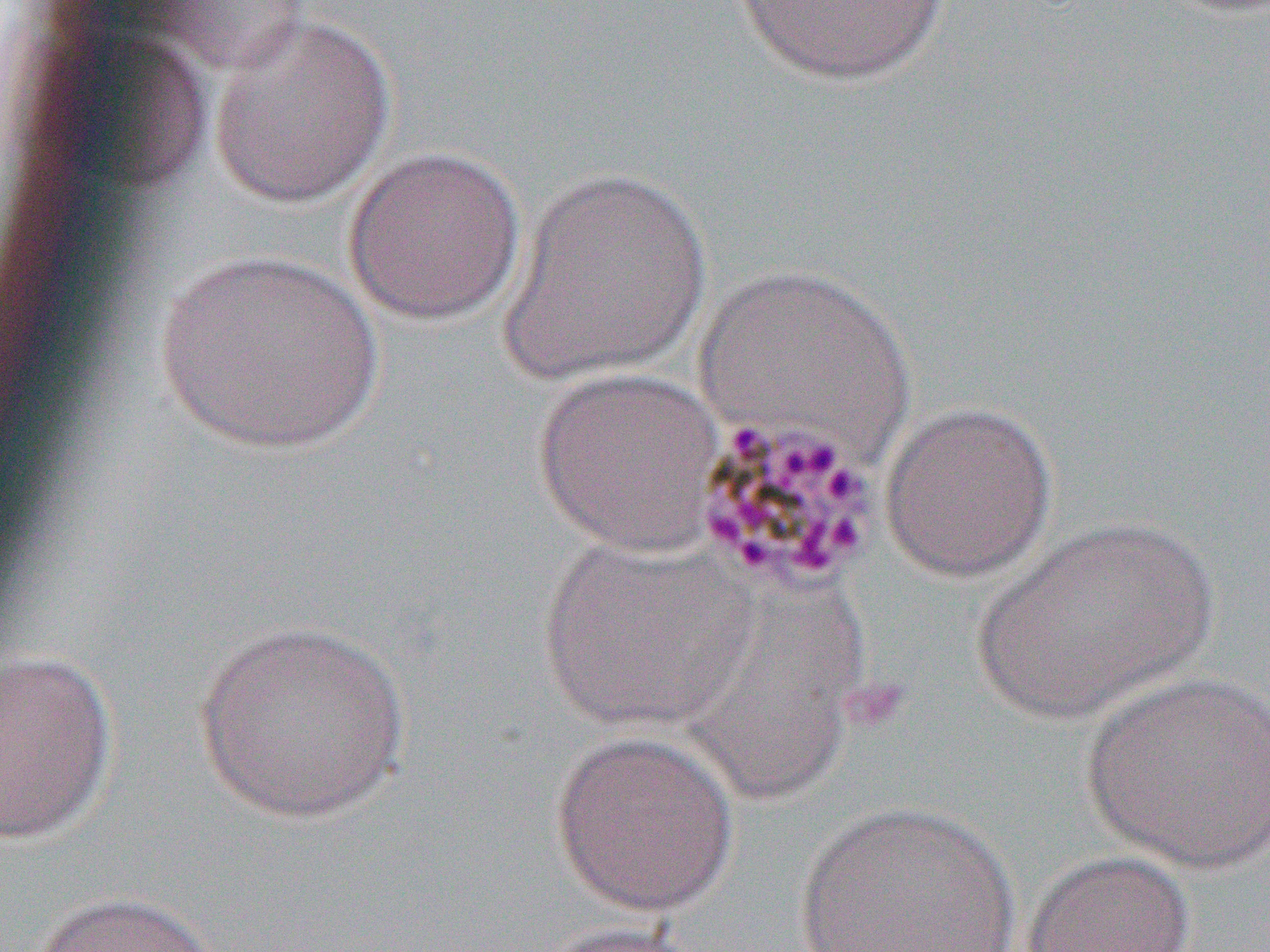

Summary:
  - Coordinate format: approximate bounding boxes as named x1/y1/x2/y2 corners in pixels
  - Uninfected red blood cell locations: (x1=729, y1=0, x2=951, y2=86), (x1=207, y1=13, x2=396, y2=209), (x1=342, y1=145, x2=528, y2=326), (x1=500, y1=163, x2=712, y2=386), (x1=151, y1=250, x2=386, y2=453), (x1=695, y1=263, x2=915, y2=466), (x1=533, y1=366, x2=726, y2=557), (x1=878, y1=399, x2=1058, y2=583), (x1=971, y1=516, x2=1219, y2=723), (x1=537, y1=533, x2=759, y2=731), (x1=194, y1=619, x2=410, y2=824), (x1=1, y1=649, x2=119, y2=845), (x1=1079, y1=670, x2=1270, y2=872), (x1=548, y1=729, x2=741, y2=916), (x1=791, y1=800, x2=1022, y2=951), (x1=1022, y1=849, x2=1197, y2=952), (x1=25, y1=890, x2=228, y2=952), (x1=532, y1=920, x2=708, y2=952)
  - Slide-level diagnosis: Plasmodium malariae
  - Image size: 1270×952 pixels
  - Magnification: 1000x
  - Modality: light microscopy
  - Field of view: one of a larger specimen
  - Preparation: thin blood film